Assess this cell for malaria.
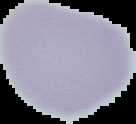

It is uninfected.

preparation = thin blood smear
image size = 136×124 pixels
image type = segmented cell region on a black background